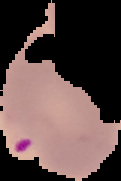

image_size: 121×181 pixels
image_type: cell region segmented out of the field of view; surrounding area masked to black
preparation: thin blood smear
malaria_status: parasitized